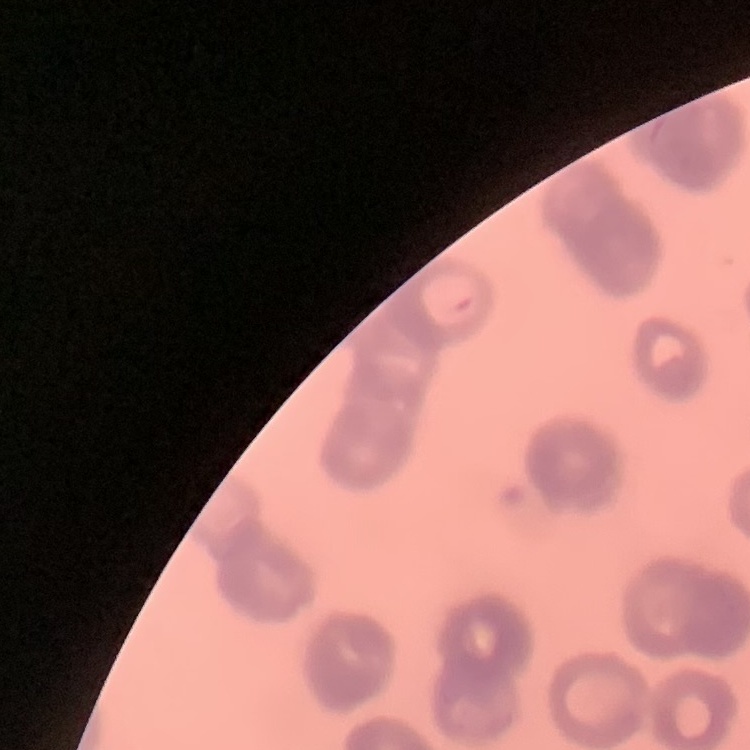
erythrocyte morphology = rouleaux formation
preparation = thin blood film
image type = square crop of a larger photomicrograph
stain = Field's or Giemsa